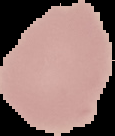

Image is 115×136 pixels. Segmented cell region on a black background. From a thin blood smear. Result: negative for malaria parasites.